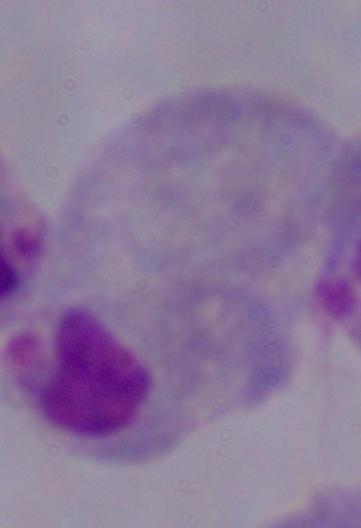

Summary:
  - Magnification: 1000x
  - Modality: photomicrograph
  - Identification: trichomonad